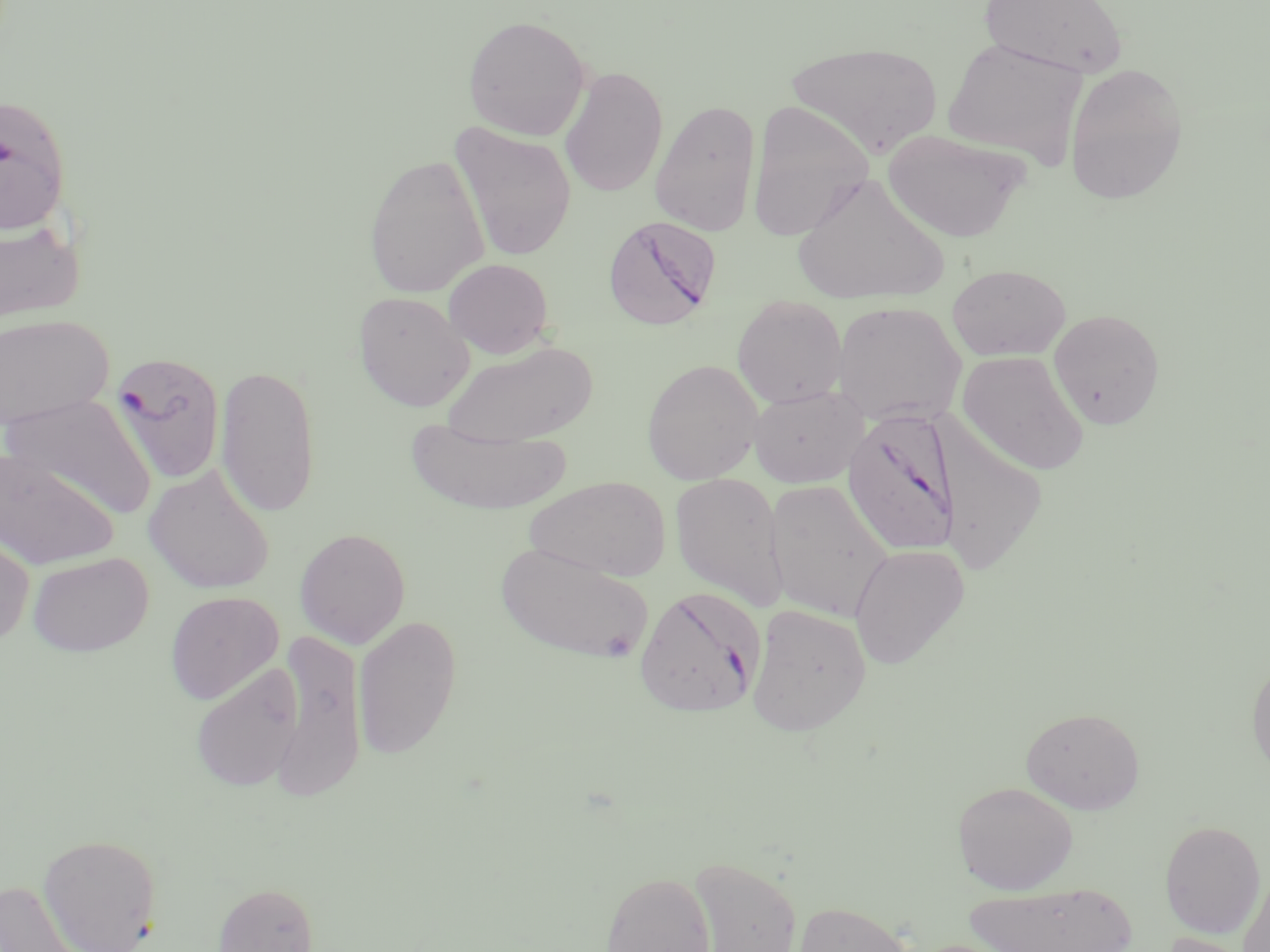

Approximate bounding boxes as (x1,y1)-(x2,y2) corner pairs in pixels. Plasmodium falciparum-infected red blood cell locations: (0,93)-(72,235), (603,215)-(722,331), (108,349)-(227,486), (842,408)-(962,555), (634,586)-(765,719). Uninfected red blood cell locations: (979,0)-(1129,78), (462,15)-(591,140), (941,38)-(1087,171), (787,41)-(942,157), (1063,62)-(1189,206), (560,66)-(668,197), (650,99)-(762,236), (746,101)-(875,242), (449,122)-(577,261), (883,129)-(1030,242), (363,153)-(489,298), (793,173)-(951,306), (0,217)-(86,325), (443,258)-(554,358), (947,263)-(1071,361), (353,291)-(475,412), (731,296)-(848,407), (832,301)-(966,427), (1048,308)-(1166,430), (1,314)-(113,431), (444,340)-(599,448), (957,350)-(1089,475), (641,359)-(763,484), (216,363)-(320,519), (747,385)-(868,488), (4,393)-(158,520), (405,417)-(573,515), (935,421)-(1048,575), (0,450)-(118,570), (144,464)-(275,594), (670,471)-(788,610), (525,476)-(670,581), (764,478)-(893,622), (0,526)-(35,649), (294,527)-(411,648), (495,541)-(655,664), (849,543)-(970,669), (28,552)-(153,656), (165,591)-(283,705), (746,604)-(872,735), (353,614)-(462,761), (270,631)-(366,803), (1247,656)-(1270,781), (190,664)-(305,792), (1020,707)-(1144,814), (953,782)-(1078,894), (1160,820)-(1266,938), (38,833)-(163,952), (689,856)-(801,952), (600,870)-(715,952), (1238,870)-(1270,952), (0,880)-(80,951), (213,881)-(319,952), (963,881)-(1138,952), (793,901)-(915,952), (1161,933)-(1257,952). Slide-level diagnosis: Plasmodium falciparum. May-Grünwald-Giemsa stain. Captured at 1000x magnification. Thin blood smear. Single field of view. Image is 1270×952 pixels. Light microscopy.